Describe the morphology of the erythrocytes.
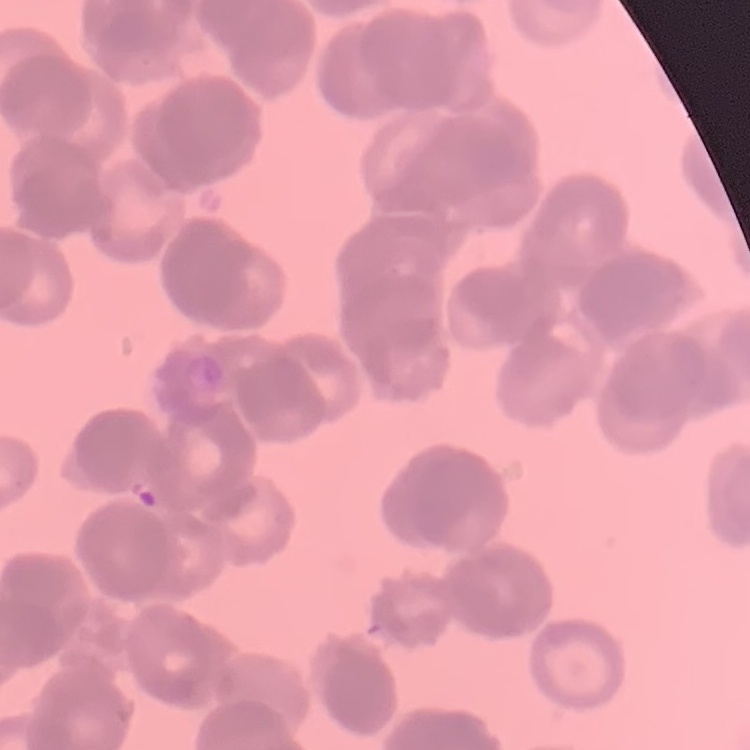
They show rouleaux formation.

Stained with either Field's or Giemsa. Square crop of a larger photomicrograph. Thin blood smear.